Locate and identify every blood parasite.
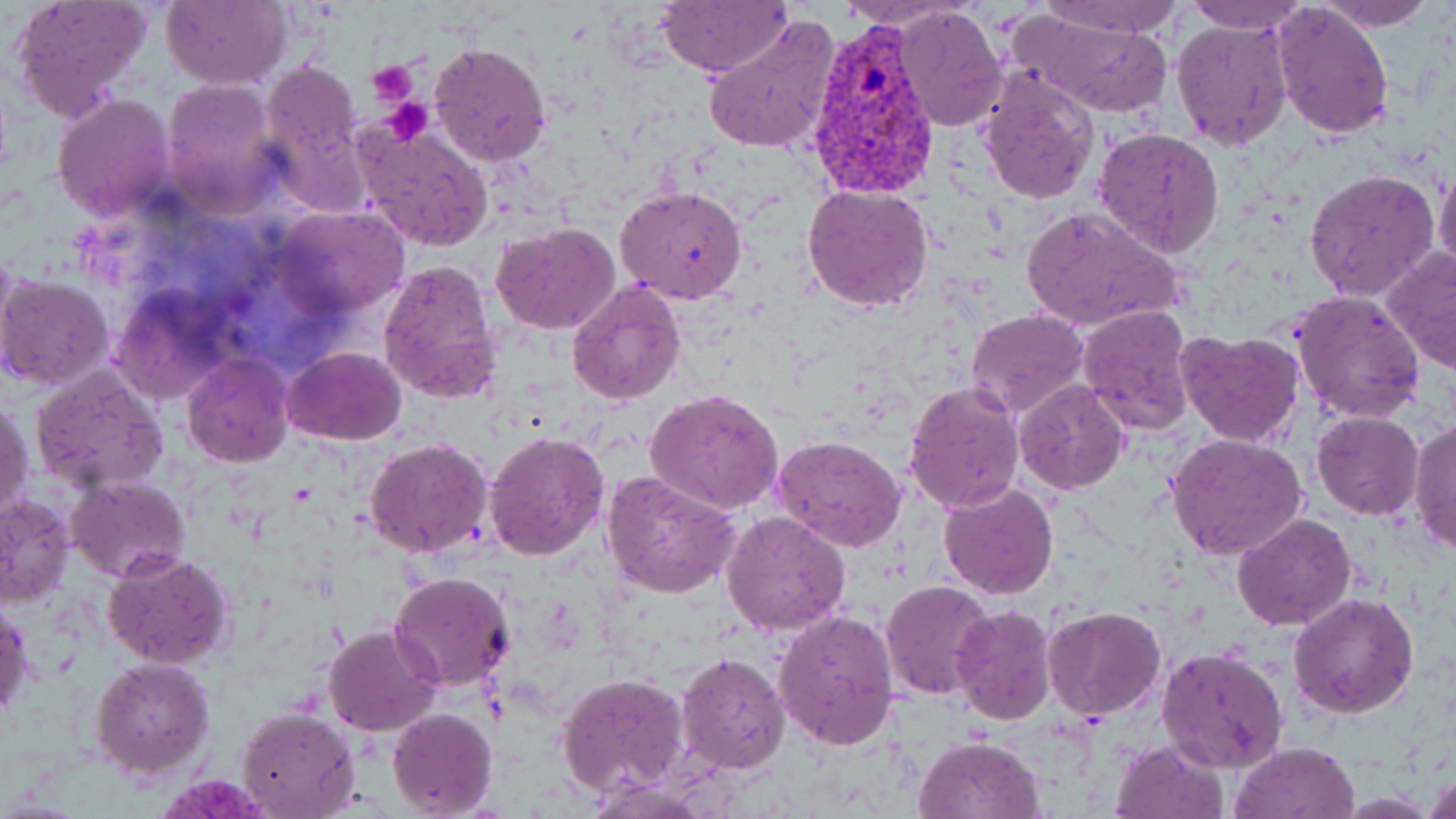
Approximate bounding boxes as (x1, y1, x2, y2) in pixels.
Plasmodium vivax-infected red blood cells: (802, 24, 941, 197).
No Plasmodium falciparum, Plasmodium ovale, Plasmodium malariae, Babesia divergens, or Trypanosoma brucei observed.

Summary:
  - Uninfected red blood cell locations: (7, 0, 151, 122), (162, 0, 291, 89), (1038, 0, 1183, 37), (1310, 0, 1440, 30), (653, 1, 792, 76), (1182, 1, 1310, 34), (1272, 3, 1395, 139), (893, 5, 1006, 132), (1007, 8, 1177, 118), (701, 13, 840, 156), (1171, 17, 1293, 151), (429, 42, 552, 166), (261, 62, 361, 173), (976, 69, 1100, 205), (160, 78, 283, 215), (51, 93, 177, 222), (354, 122, 495, 253), (1092, 127, 1225, 260), (1434, 163, 1456, 282), (1304, 169, 1441, 301), (615, 184, 748, 303), (802, 184, 935, 313), (1018, 204, 1186, 335), (274, 207, 410, 315), (492, 222, 621, 334), (1384, 247, 1456, 375), (376, 259, 504, 406), (0, 275, 114, 391), (566, 280, 686, 405), (113, 288, 232, 406), (1293, 291, 1425, 425), (1077, 304, 1197, 435), (966, 308, 1088, 418), (1175, 327, 1305, 448), (283, 348, 406, 445), (181, 352, 293, 466), (30, 366, 168, 493), (1014, 380, 1128, 494), (904, 381, 1025, 512), (645, 388, 785, 516), (1, 396, 33, 522), (1311, 410, 1424, 520), (1409, 420, 1456, 554), (483, 429, 608, 561), (1166, 432, 1308, 560), (774, 434, 908, 553), (366, 437, 494, 555), (602, 471, 742, 598), (66, 476, 191, 583), (937, 482, 1058, 601), (0, 494, 73, 605), (721, 511, 852, 636), (1232, 512, 1357, 632), (102, 548, 235, 671), (390, 571, 515, 691), (881, 580, 995, 700), (1288, 592, 1420, 720), (1, 595, 33, 724), (949, 604, 1055, 724), (1041, 606, 1167, 719), (773, 608, 899, 749), (323, 624, 443, 736), (1158, 647, 1289, 775), (676, 650, 791, 775), (90, 657, 215, 775), (557, 673, 687, 796), (236, 706, 360, 819), (387, 707, 497, 818), (912, 735, 1044, 819), (1109, 737, 1231, 819), (1230, 741, 1360, 819), (1424, 772, 1456, 819)
  - Platelet locations: (368, 62, 420, 107), (381, 97, 434, 145)
  - Slide-level diagnosis: Plasmodium vivax
  - Modality: light microscopy
  - Field of view: single
  - Magnification: 1000x
  - Stain: May-Grünwald-Giemsa
  - Preparation: thin blood film
  - Image size: 1456×819 pixels